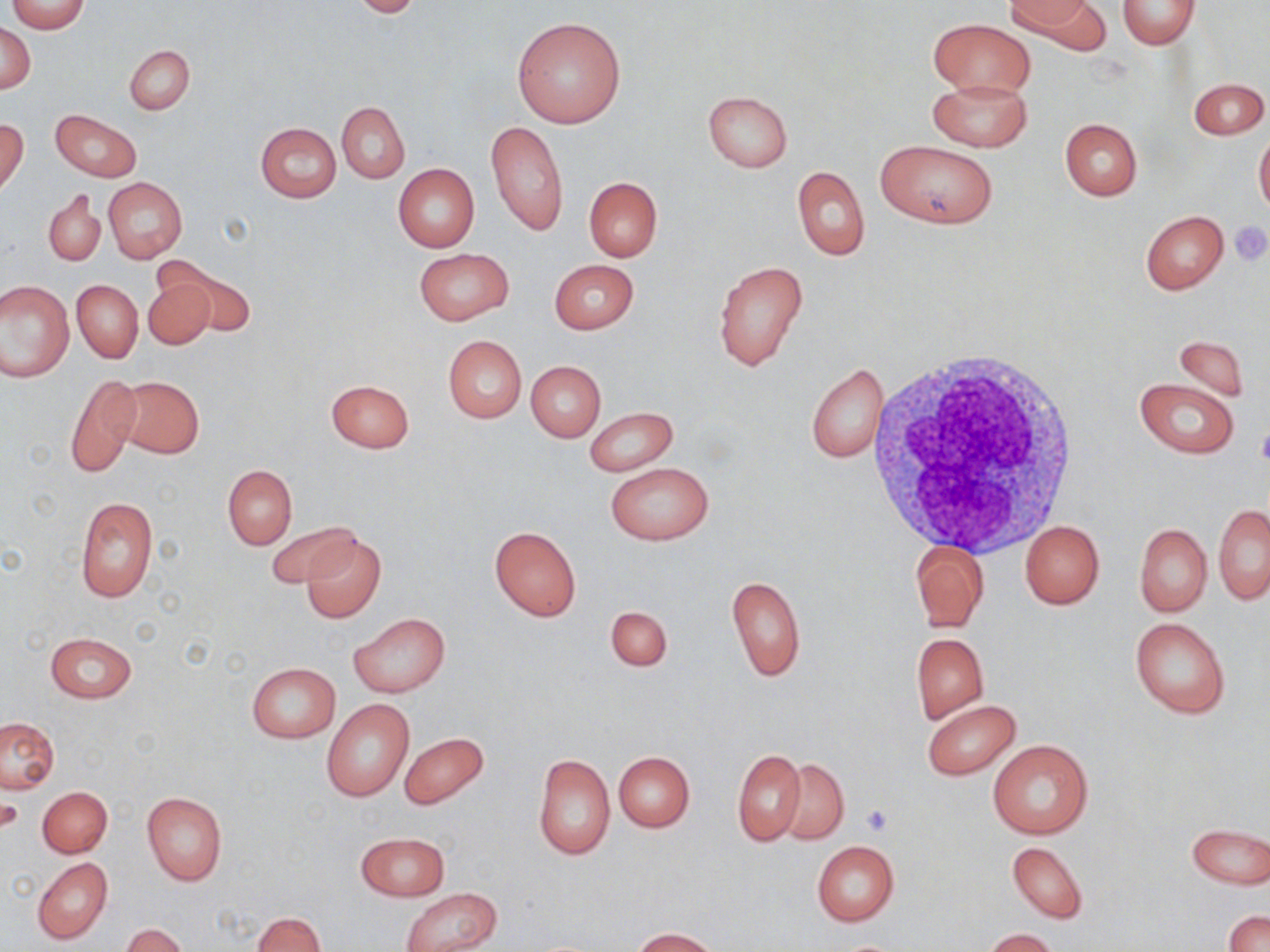
Summary:
  - Coordinate format: approximate bounding boxes as (x1, y1, x2, y2) in pixels
  - Uninfected red blood cell locations: (9, 0, 88, 32), (348, 0, 426, 17), (1009, 0, 1107, 53), (1116, 0, 1199, 49), (512, 17, 626, 128), (928, 18, 1036, 98), (1, 22, 35, 93), (125, 44, 194, 115), (927, 78, 1033, 152), (1189, 78, 1268, 139), (701, 90, 792, 171), (337, 102, 408, 183), (51, 110, 141, 182), (1, 118, 29, 195), (1059, 118, 1142, 200), (485, 121, 568, 236), (255, 122, 341, 201), (1254, 126, 1270, 218), (877, 141, 998, 229), (393, 163, 479, 253), (792, 166, 870, 262), (584, 177, 663, 262), (105, 178, 187, 262), (45, 188, 106, 266), (1140, 211, 1227, 294), (413, 248, 514, 325), (549, 259, 639, 335), (715, 260, 807, 372), (175, 265, 255, 336), (142, 275, 216, 350), (1, 280, 74, 380), (71, 280, 142, 362), (1173, 334, 1249, 403), (443, 336, 526, 422), (526, 361, 605, 441), (805, 363, 889, 463), (64, 373, 141, 479), (115, 375, 204, 458), (1133, 377, 1240, 458), (324, 379, 414, 453), (582, 407, 678, 477), (605, 462, 714, 546), (223, 466, 297, 549), (75, 496, 157, 603), (1213, 504, 1269, 605), (265, 520, 356, 588), (1019, 520, 1105, 610), (1135, 523, 1211, 617), (489, 527, 582, 620), (301, 533, 386, 622), (910, 539, 987, 631), (727, 574, 806, 683), (605, 606, 673, 672), (349, 612, 451, 697), (1129, 616, 1231, 719), (44, 632, 137, 704), (911, 633, 989, 723), (246, 662, 341, 742), (922, 699, 1021, 780), (321, 700, 415, 802), (1, 717, 59, 793), (400, 731, 489, 810), (987, 739, 1094, 841), (732, 748, 806, 845), (613, 751, 695, 832), (533, 753, 615, 860), (773, 760, 849, 844), (38, 786, 112, 857), (142, 792, 227, 885), (3, 794, 23, 837), (1185, 824, 1270, 889), (355, 832, 449, 900), (811, 841, 899, 927), (1006, 841, 1089, 924), (32, 858, 112, 944), (401, 887, 503, 952), (1224, 911, 1269, 952), (252, 912, 325, 951), (120, 924, 190, 952), (630, 928, 720, 952), (982, 928, 1059, 952)
  - Platelet locations: (1228, 221, 1270, 265), (1257, 423, 1270, 468), (1, 794, 24, 835), (863, 805, 892, 836)
  - White blood cell locations: (865, 345, 1084, 559)
  - Slide-level diagnosis: no evidence of blood parasites
  - Field of view: one of a larger specimen
  - Modality: optical microscopy
  - Image size: 1270×952 pixels
  - Magnification: 1000x
  - Stain: May-Grünwald-Giemsa
  - Preparation: thin blood smear